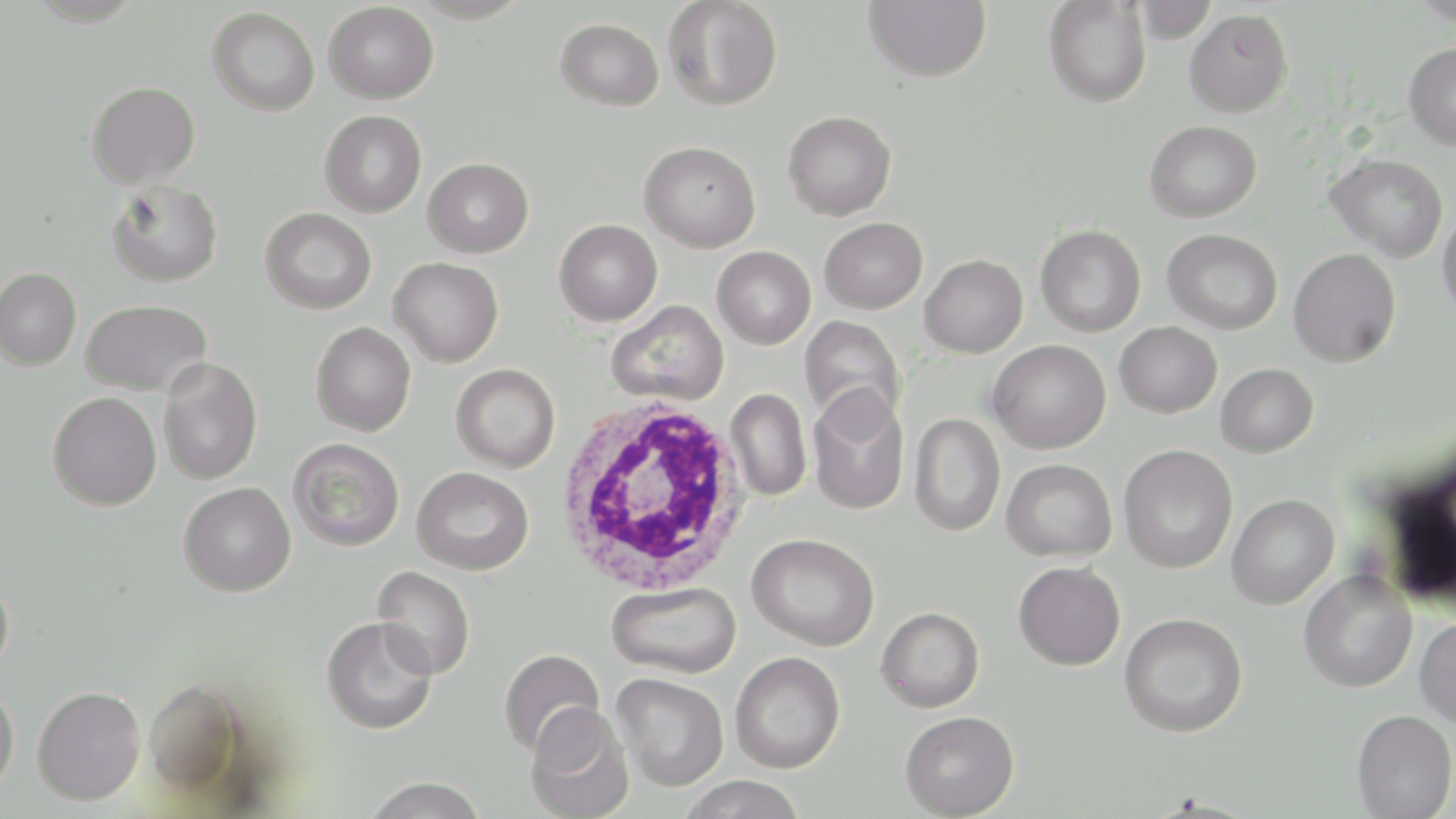

slide-level diagnosis = Plasmodium falciparum
uninfected red blood cell locations = approximate bounding boxes as [x1, y1, x2, y2] in pixels: [663, 0, 783, 111], [862, 0, 991, 82], [1411, 0, 1456, 26], [1043, 1, 1151, 107], [1133, 1, 1219, 42], [324, 2, 439, 104], [207, 6, 320, 116], [1184, 8, 1294, 117], [555, 18, 664, 111], [1403, 42, 1456, 149], [86, 81, 200, 188], [320, 110, 427, 217], [783, 110, 897, 220], [1145, 120, 1262, 222], [639, 141, 761, 252], [1326, 153, 1448, 262], [423, 157, 534, 258], [107, 179, 223, 287], [260, 207, 376, 314], [1437, 210, 1456, 320], [819, 217, 927, 314], [554, 219, 662, 325], [1036, 224, 1146, 337], [1162, 228, 1282, 334], [712, 245, 815, 349], [1288, 248, 1400, 367], [920, 254, 1027, 357], [389, 257, 503, 367], [0, 267, 81, 370], [80, 300, 212, 395], [607, 300, 728, 406], [799, 316, 906, 427], [1115, 321, 1222, 417], [311, 322, 416, 436], [988, 339, 1111, 454], [158, 358, 263, 484], [451, 363, 560, 472], [1216, 363, 1318, 457], [806, 385, 910, 515], [726, 388, 811, 501], [47, 391, 162, 511], [909, 413, 1005, 537], [288, 437, 405, 551], [1118, 444, 1238, 573], [1002, 458, 1117, 562], [411, 466, 534, 575], [179, 482, 296, 596], [1226, 494, 1339, 609], [747, 533, 880, 651], [1014, 561, 1125, 669], [373, 566, 475, 679], [1299, 570, 1417, 692], [0, 572, 14, 679], [606, 580, 742, 679], [876, 606, 984, 713], [1119, 612, 1248, 737], [321, 616, 438, 735], [1414, 616, 1456, 727], [498, 648, 606, 756], [729, 651, 845, 773], [611, 672, 728, 791], [144, 678, 248, 794], [0, 683, 19, 795], [32, 685, 145, 805], [525, 704, 634, 819], [1352, 709, 1456, 818], [900, 711, 1019, 818], [677, 775, 808, 819], [363, 776, 487, 818]
modality = light microscopy
white blood cell locations = approximate bounding boxes as [x1, y1, x2, y2] in pixels: [554, 396, 750, 596]
preparation = thin blood smear
magnification = 1000x
stain = May-Grünwald-Giemsa
field of view = one of a larger specimen
image size = 1456×819 pixels